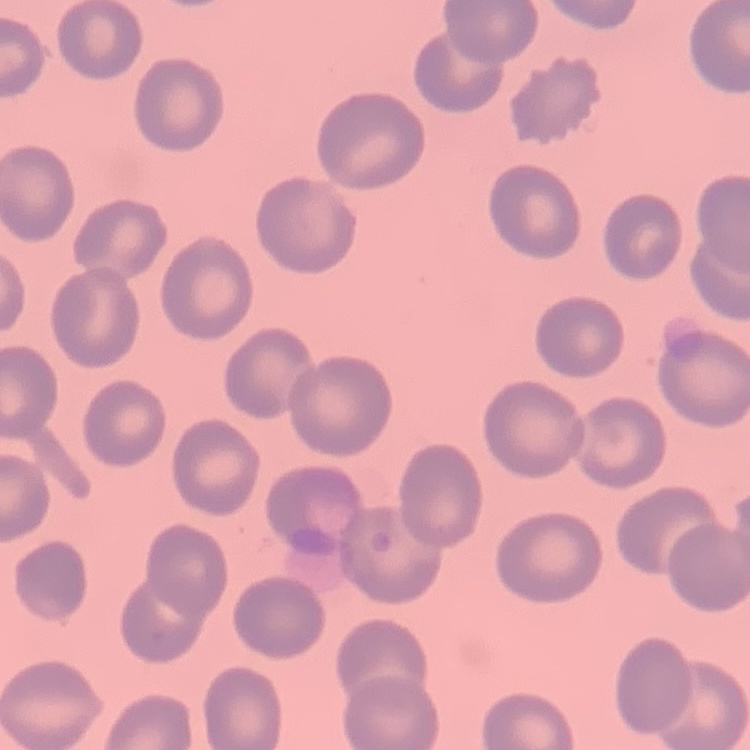
Summary:
  - Red blood cell morphology: no rouleaux formation
  - Stain: Field's or Giemsa
  - Image type: square crop of a larger photomicrograph
  - Preparation: thin blood film